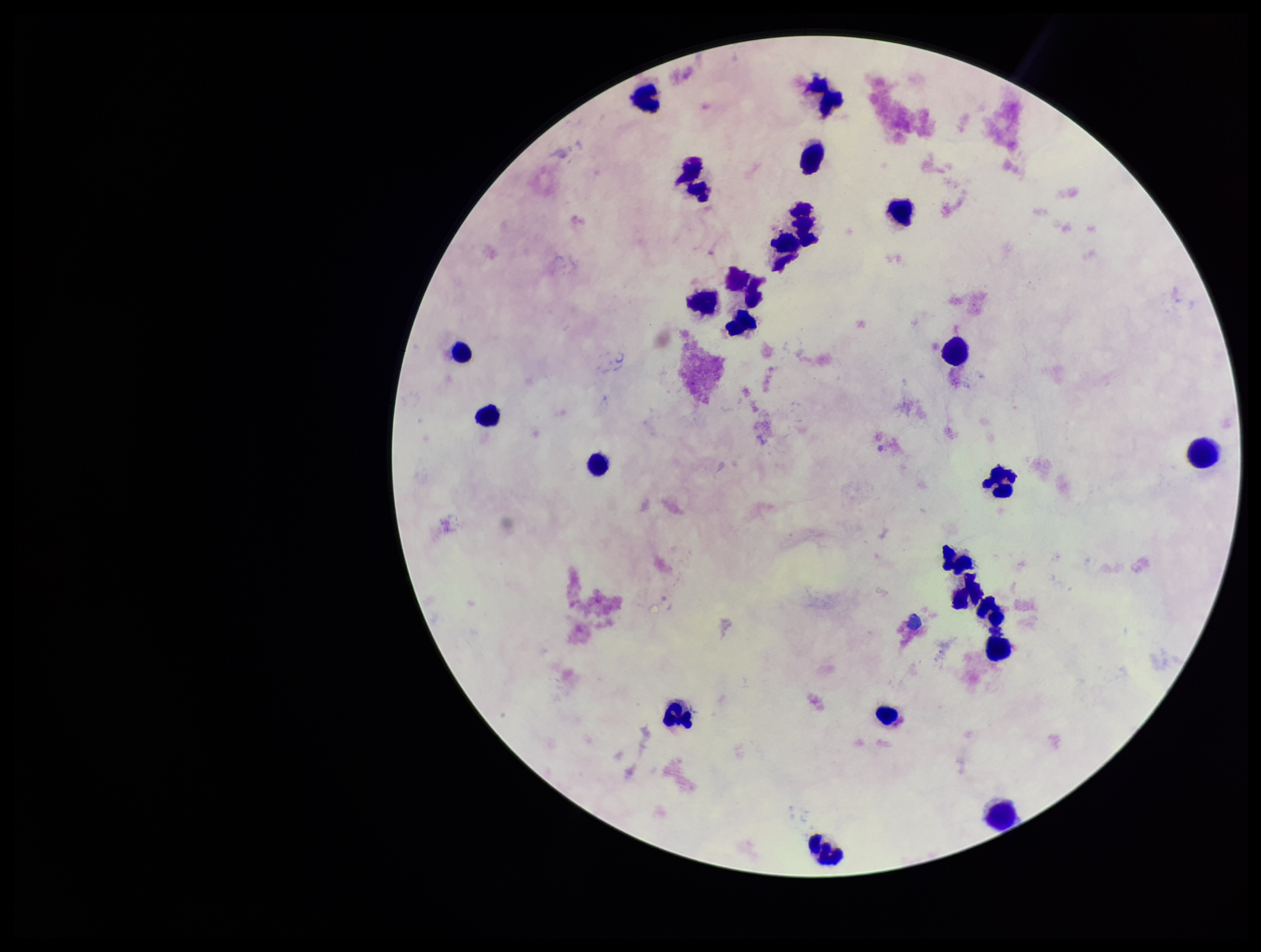
Summary:
  - Plasmodium parasites: none detected
  - Patient malaria status: negative
  - Leukocyte count: 24
  - Preparation: thick
  - Field of view: one from this slide
  - Capture: smartphone photograph through the microscope eyepiece
  - Image size: 1261×952 pixels
  - Parasite count: 0
  - Stain: Giemsa